Classify this cell by malaria status.
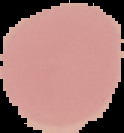

Uninfected.

Cell region segmented out of the field of view; the surrounding area is masked to black. Image is 124×133 pixels. From a thin blood film.